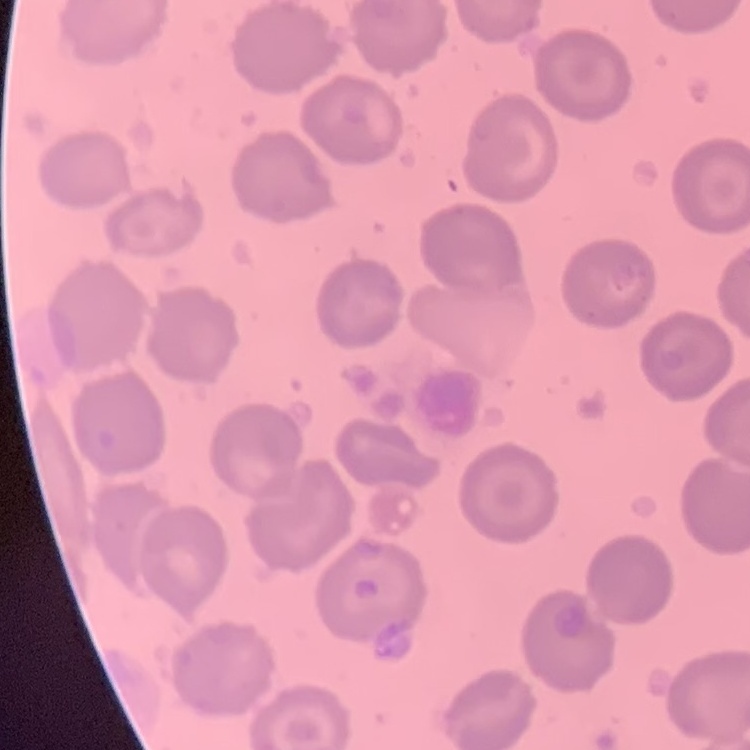
Summary:
  - Red blood cell morphology: no rouleaux formation
  - Image type: square crop of a larger photomicrograph
  - Stain: Field's or Giemsa
  - Preparation: thin blood film